Report the malaria status of this cell.
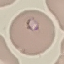
It is parasitized.

Summary:
  - Stain: Giemsa
  - Preparation: thin smear
  - Capture: smartphone camera at the microscope eyepiece
  - Image type: cell patch, automatically extracted from a larger field of view and resized to 64 × 64 pixels